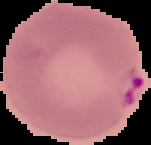
image size = 151×145 pixels
preparation = thin blood smear
malaria status = parasitized
image type = cell region segmented out of the field of view; surrounding area masked to black